Outline every trophozoite.
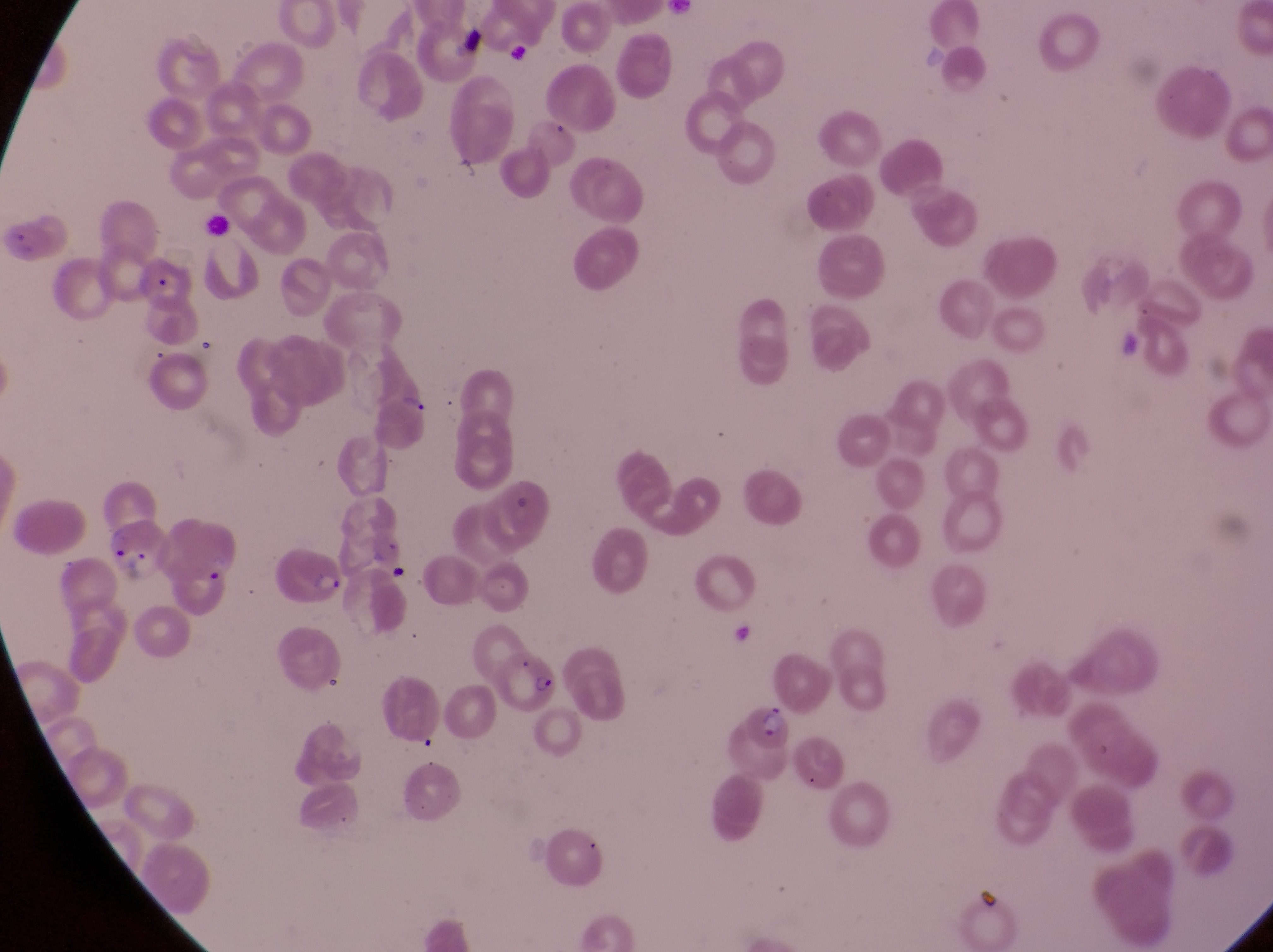
Approximate bounding boxes as left top right bottom in pixels.
Trophozoites: 395 384 437 419.

country: Uganda
field_of_view: single
preparation: thin blood film
image_size: 1273×952 pixels
artifact_platelet_like_body_stain_precipitate_or_debris_locations: 'approximate bounding boxes as left top right bottom in pixels: 451 22 498 69'
magnification: 1000x
parasitised_red_blood_cell_locations: 'approximate bounding boxes as left top right bottom in pixels: 4 211 73 263; 134 253 206 311; 102 522 164 580; 270 554 352 609; 502 639 557 716; 741 699 793 766'
capture: smartphone photograph through the eyepiece of an Olympus CX-23 microscope